Name the cell type shown.
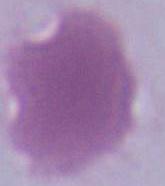

An erythrocyte.

{
  "modality": "micrograph",
  "magnification": "1000x"
}